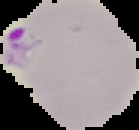

Image is 139×130 pixels. From a thin blood film. Malaria status: parasitized. The area outside the segmented cell region is set to black.